Name the parasite shown.
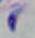

This is Toxoplasma gondii.

Micrograph. 1000x magnification.